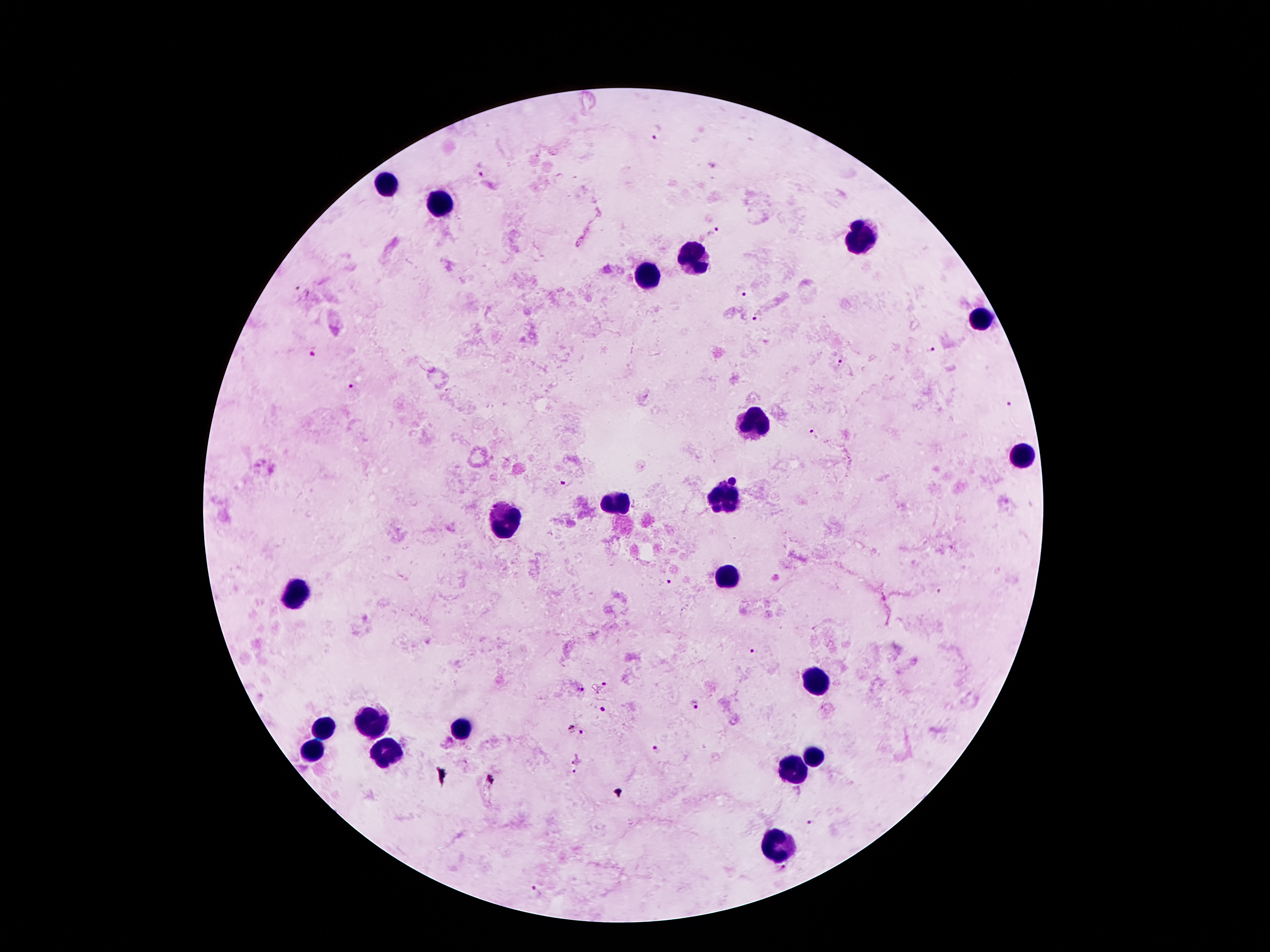
Approximate object centers, in pixels from the top-left corner. Plasmodium parasite locations: (x=655, y=132), (x=481, y=174), (x=712, y=232), (x=739, y=292), (x=757, y=318), (x=313, y=350), (x=930, y=350), (x=838, y=363), (x=352, y=387), (x=1008, y=403), (x=814, y=434), (x=568, y=481), (x=670, y=584), (x=752, y=652), (x=605, y=683), (x=579, y=687), (x=696, y=705), (x=604, y=708), (x=571, y=726), (x=581, y=733), (x=657, y=749), (x=575, y=759), (x=572, y=772), (x=814, y=823), (x=536, y=893). Leukocyte locations: (x=383, y=184), (x=441, y=204), (x=863, y=239), (x=697, y=257), (x=648, y=274), (x=986, y=321), (x=750, y=423), (x=1023, y=452), (x=728, y=495), (x=617, y=501), (x=504, y=524), (x=726, y=575), (x=295, y=591), (x=818, y=682), (x=365, y=722), (x=324, y=729), (x=459, y=729), (x=312, y=751), (x=389, y=751), (x=816, y=753), (x=793, y=772), (x=781, y=847). Giemsa-stained preparation. Single field of view. 100x magnification. Image is 1270×952 pixels. Patient malaria status: infected with Plasmodium falciparum. Thick peripheral-blood smear. Photographed through the microscope eyepiece with a smartphone camera.